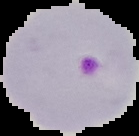
Summary:
  - Image size: 139×136 pixels
  - Image type: segmented cell region on a black background
  - Preparation: thin blood film
  - Result: Plasmodium parasites identified